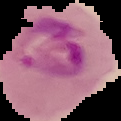
Summary:
  - Image size: 121×121 pixels
  - Malaria status: parasitized
  - Image type: segmented cell region with the area outside set to black
  - Preparation: thin blood film